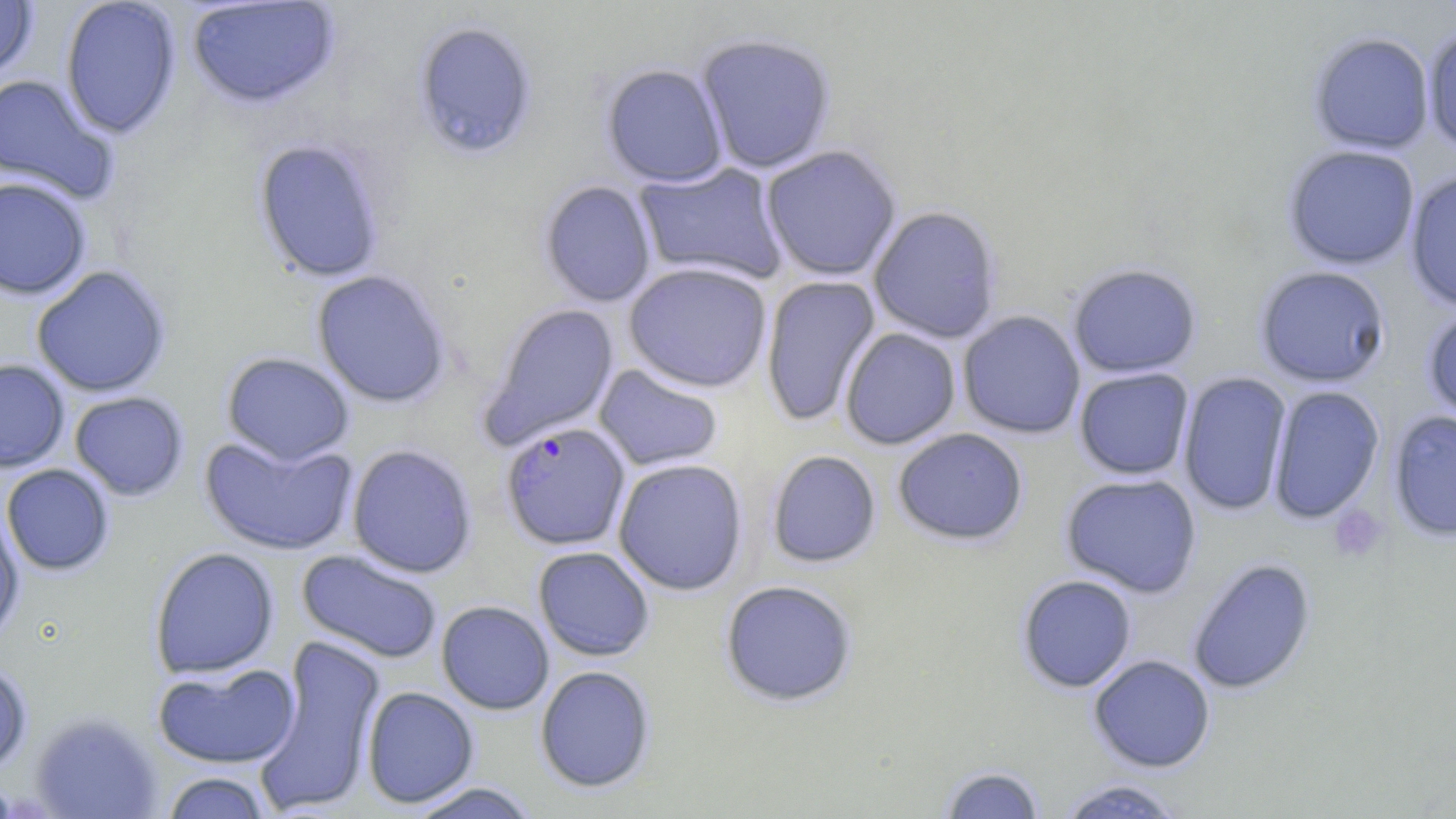

Summary:
  - Coordinate format: approximate bounding boxes as [x1, y1, x2, y2] in pixels
  - Platelet locations: [1328, 506, 1387, 563]
  - Uninfected red blood cell locations: [60, 0, 182, 140], [185, 1, 340, 110], [0, 2, 39, 84], [412, 21, 538, 161], [1422, 25, 1456, 155], [1308, 31, 1435, 155], [695, 33, 836, 174], [601, 63, 729, 187], [0, 74, 116, 204], [253, 139, 388, 283], [760, 145, 903, 281], [1282, 145, 1421, 270], [634, 162, 789, 286], [1403, 170, 1456, 313], [0, 177, 92, 300], [538, 180, 657, 308], [867, 205, 1003, 344], [623, 262, 773, 393], [1067, 263, 1202, 378], [31, 265, 173, 398], [1254, 265, 1391, 388], [311, 269, 452, 408], [760, 275, 881, 428], [481, 303, 621, 448], [1421, 305, 1456, 427], [957, 310, 1086, 439], [840, 327, 962, 450], [221, 352, 355, 465], [0, 359, 70, 473], [593, 363, 724, 472], [1073, 367, 1195, 480], [1177, 372, 1293, 516], [1266, 385, 1385, 523], [69, 391, 190, 502], [1388, 409, 1456, 543], [892, 428, 1029, 546], [199, 434, 358, 557], [347, 444, 478, 579], [766, 450, 882, 569], [612, 458, 749, 596], [1, 464, 115, 576], [1060, 472, 1202, 598], [0, 506, 25, 645], [533, 546, 655, 662], [149, 547, 280, 679], [296, 548, 443, 664], [1187, 557, 1316, 695], [1016, 574, 1137, 693], [719, 579, 859, 707], [436, 600, 554, 715], [253, 634, 386, 816], [1088, 654, 1216, 773], [0, 662, 34, 777], [153, 662, 300, 769], [534, 666, 656, 794], [362, 686, 479, 808], [30, 713, 162, 819], [936, 764, 1047, 819], [159, 771, 272, 818], [1054, 778, 1188, 818], [404, 781, 542, 819]
  - Plasmodium falciparum-infected red blood cell locations: [500, 422, 631, 551]
  - Slide-level diagnosis: Plasmodium falciparum
  - Preparation: thin blood smear
  - Magnification: 1000x
  - Image size: 1456×819 pixels
  - Field of view: single
  - Stain: May-Grünwald-Giemsa
  - Modality: light microscopy